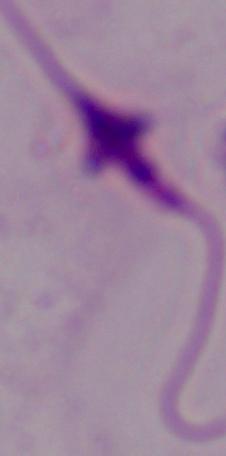
A Leishmania parasite is seen. Captured at 1000x magnification. Micrograph.